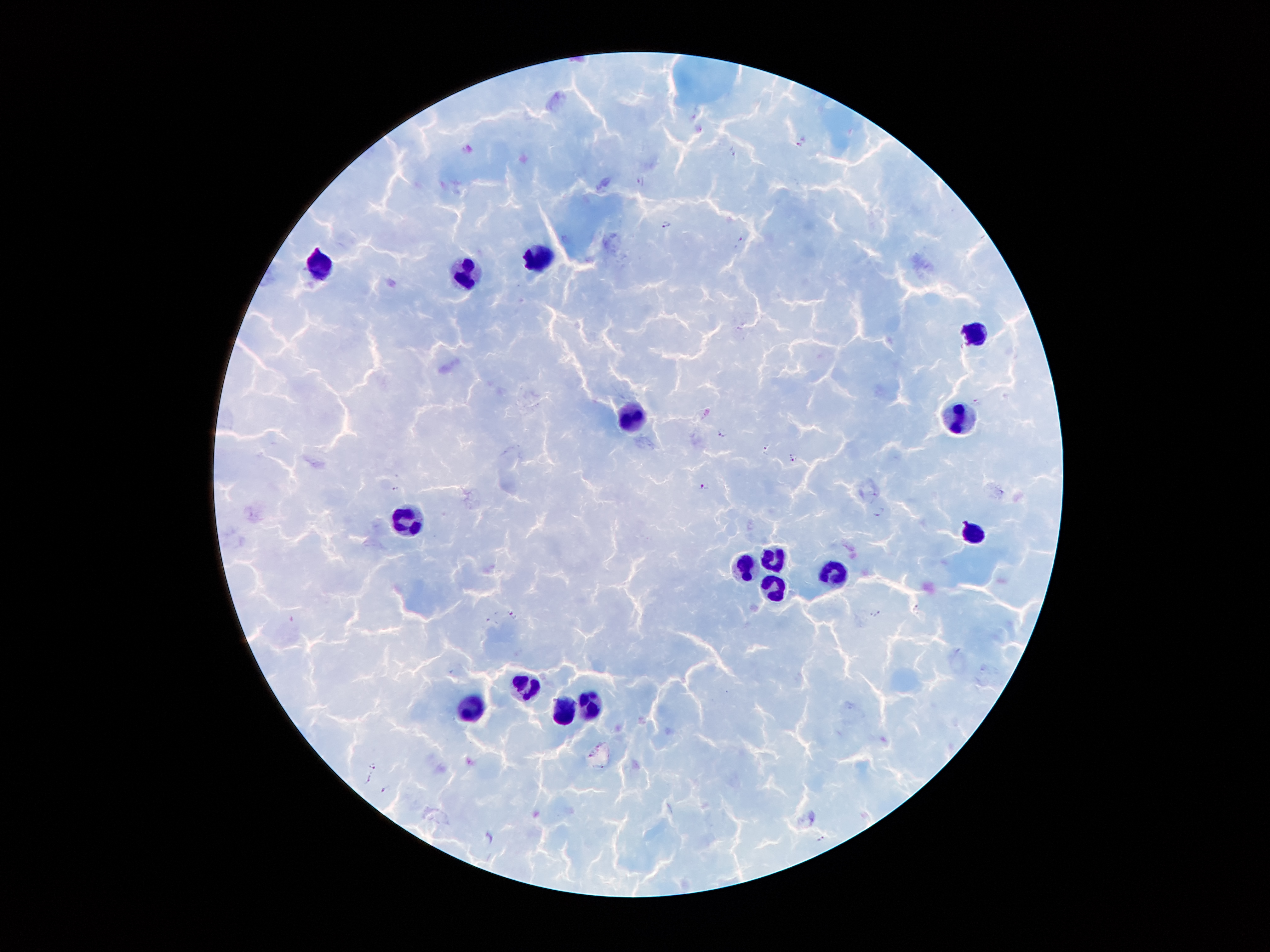 Approximate centers as {x, y} in pixels. Malaria parasite locations: {803, 142}, {733, 151}, {640, 180}, {666, 223}, {741, 240}, {977, 401}, {721, 434}, {765, 447}, {793, 457}, {704, 487}, {396, 489}, {1001, 492}, {878, 511}, {916, 609}, {513, 613}, {875, 614}, {373, 765}, {369, 779}, {385, 789}, {820, 839}. Leukocyte locations: {538, 257}, {320, 265}, {464, 274}, {979, 333}, {634, 415}, {961, 415}, {403, 519}, {970, 533}, {776, 559}, {741, 566}, {834, 575}, {775, 585}, {525, 687}, {588, 703}, {563, 711}, {471, 712}. One field from this slide. Photographed through the microscope eyepiece with a smartphone camera. Image is 1270×952 pixels. Thick peripheral-blood smear. Patient malaria status: infected with Plasmodium falciparum. 100x magnification. Giemsa stain.